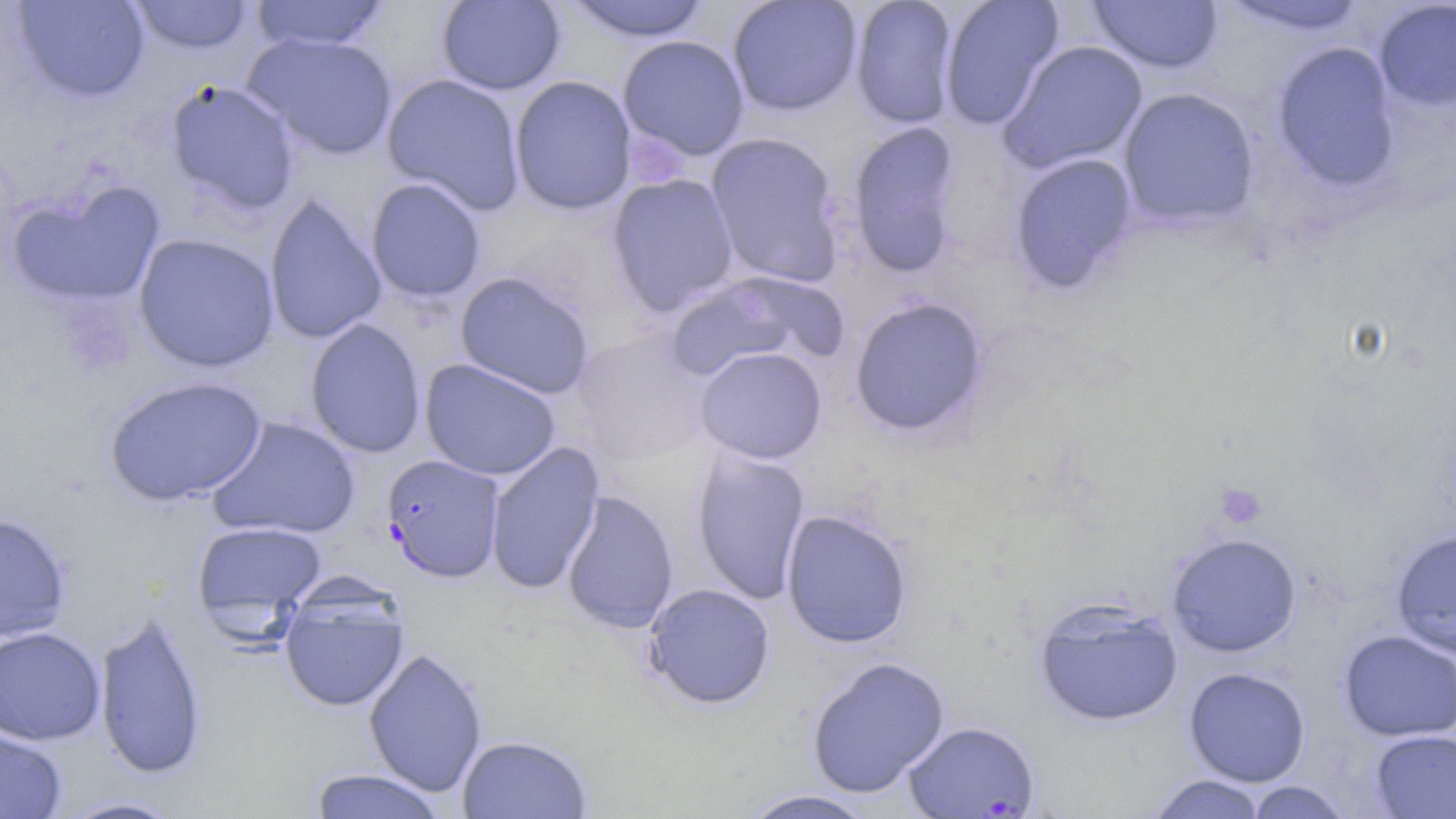
Approximate bounding boxes as named x1/y1/x2/y2 corners in pixels. Uninfected red blood cell locations: (x1=11, y1=0, x2=151, y2=103), (x1=129, y1=0, x2=254, y2=56), (x1=248, y1=0, x2=391, y2=53), (x1=436, y1=0, x2=566, y2=95), (x1=561, y1=0, x2=714, y2=43), (x1=727, y1=0, x2=863, y2=117), (x1=849, y1=0, x2=959, y2=129), (x1=939, y1=0, x2=1065, y2=130), (x1=1087, y1=0, x2=1224, y2=75), (x1=1216, y1=0, x2=1372, y2=37), (x1=1373, y1=0, x2=1456, y2=112), (x1=242, y1=31, x2=399, y2=160), (x1=617, y1=35, x2=750, y2=161), (x1=998, y1=39, x2=1149, y2=175), (x1=1269, y1=41, x2=1403, y2=192), (x1=382, y1=73, x2=526, y2=214), (x1=509, y1=75, x2=637, y2=215), (x1=164, y1=79, x2=302, y2=215), (x1=1116, y1=87, x2=1260, y2=230), (x1=846, y1=120, x2=965, y2=279), (x1=705, y1=132, x2=846, y2=288), (x1=1008, y1=152, x2=1139, y2=295), (x1=606, y1=173, x2=739, y2=316), (x1=365, y1=177, x2=486, y2=303), (x1=7, y1=180, x2=166, y2=308), (x1=263, y1=193, x2=387, y2=345), (x1=133, y1=232, x2=280, y2=373), (x1=667, y1=269, x2=849, y2=382), (x1=454, y1=271, x2=595, y2=399), (x1=848, y1=296, x2=990, y2=439), (x1=304, y1=318, x2=427, y2=459), (x1=572, y1=329, x2=714, y2=465), (x1=695, y1=346, x2=827, y2=464), (x1=420, y1=358, x2=561, y2=481), (x1=103, y1=375, x2=269, y2=507), (x1=207, y1=416, x2=361, y2=540), (x1=484, y1=442, x2=605, y2=595), (x1=690, y1=446, x2=812, y2=605), (x1=560, y1=489, x2=679, y2=634), (x1=780, y1=509, x2=913, y2=649), (x1=0, y1=512, x2=72, y2=642), (x1=191, y1=521, x2=327, y2=626), (x1=1389, y1=527, x2=1456, y2=658), (x1=1166, y1=532, x2=1302, y2=657), (x1=642, y1=582, x2=776, y2=710), (x1=278, y1=589, x2=410, y2=713), (x1=1033, y1=596, x2=1184, y2=727), (x1=94, y1=609, x2=208, y2=781), (x1=0, y1=626, x2=106, y2=746), (x1=1338, y1=630, x2=1456, y2=742), (x1=363, y1=647, x2=488, y2=797), (x1=806, y1=655, x2=951, y2=799), (x1=1183, y1=666, x2=1312, y2=786), (x1=0, y1=726, x2=68, y2=819), (x1=1369, y1=729, x2=1456, y2=818), (x1=457, y1=734, x2=593, y2=819), (x1=307, y1=767, x2=448, y2=819), (x1=1146, y1=774, x2=1269, y2=818), (x1=1244, y1=780, x2=1353, y2=818), (x1=739, y1=788, x2=878, y2=819), (x1=55, y1=795, x2=188, y2=818). Platelet locations: (x1=624, y1=131, x2=689, y2=188), (x1=1214, y1=482, x2=1267, y2=529). Plasmodium falciparum-infected red blood cell locations: (x1=382, y1=454, x2=506, y2=583), (x1=902, y1=719, x2=1041, y2=818). Slide-level diagnosis: Plasmodium falciparum. Optical microscopy. Captured at 1000x magnification. Single field of view. Thin blood film. May-Grünwald-Giemsa stain. Image is 1456×819 pixels.